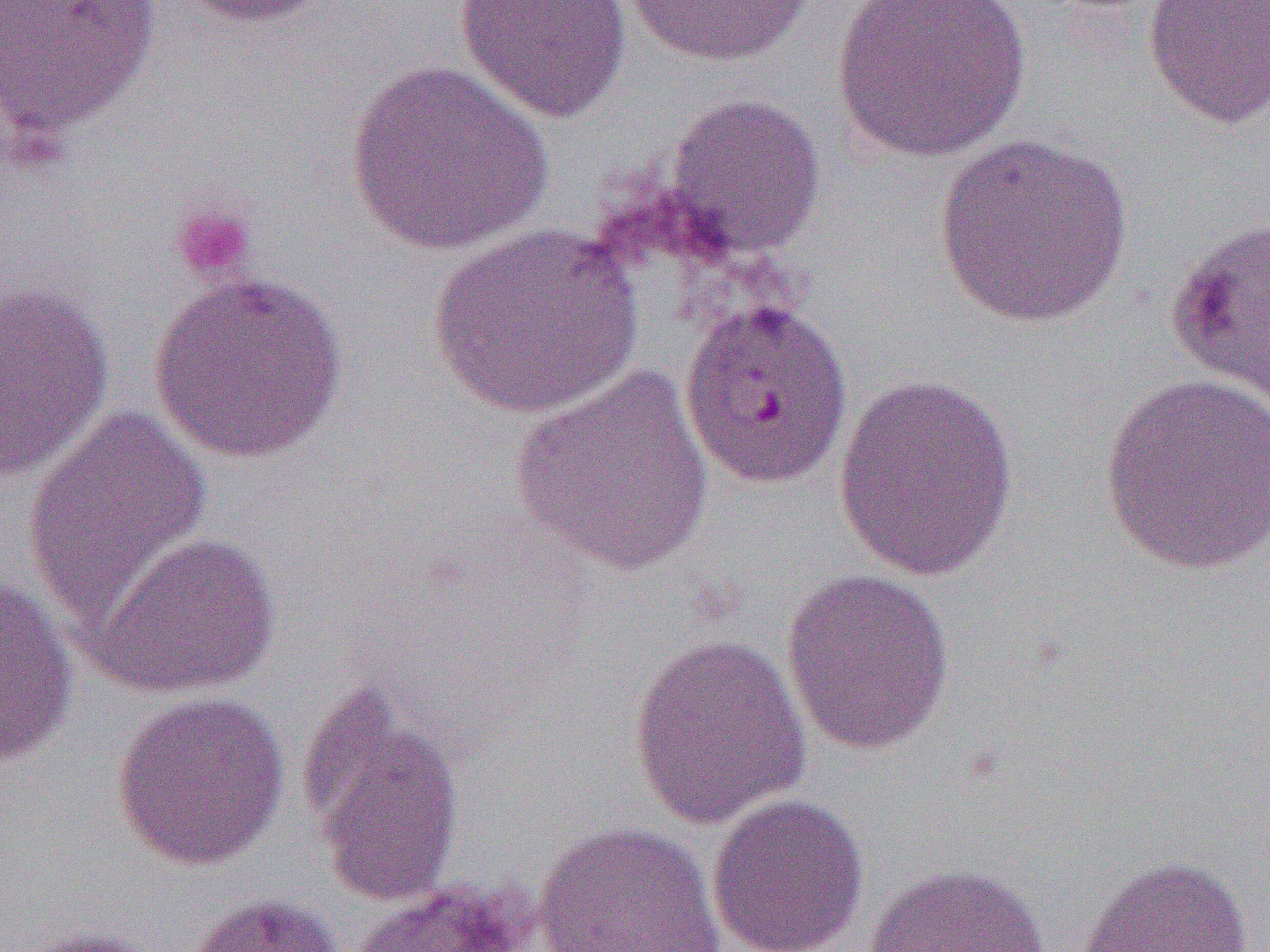

Approximate bounding boxes as (x1, y1, x2, y2) in pixels. Platelet locations: (168, 200, 259, 285). Uninfected red blood cell locations (subset): (0, 0, 163, 143), (173, 0, 340, 30), (454, 0, 631, 124), (619, 0, 818, 67), (1143, 0, 1270, 130), (828, 1, 1034, 163), (342, 58, 556, 257), (663, 92, 827, 259), (933, 132, 1134, 329), (1165, 213, 1270, 415), (425, 222, 642, 419), (147, 270, 349, 464), (0, 279, 114, 482), (509, 366, 716, 577), (832, 373, 1020, 582), (1099, 374, 1270, 575), (22, 404, 215, 629), (86, 531, 282, 700), (781, 567, 956, 755), (0, 576, 79, 770), (627, 630, 812, 830), (301, 686, 466, 908), (110, 690, 291, 871), (706, 792, 870, 952), (533, 819, 726, 952), (1073, 854, 1255, 952), (862, 861, 1053, 952), (350, 880, 533, 951), (183, 892, 346, 952), (6, 925, 163, 952). Slide-level diagnosis: Plasmodium falciparum. Image is 1270×952 pixels. Thin blood film. Single field of view. Captured at 1000x magnification. Optical microscopy.